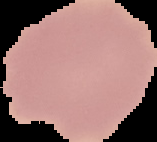

Result: no Plasmodium parasites detected. Image is 157×142 pixels. The area outside the segmented cell region is set to black. From a thin blood film.